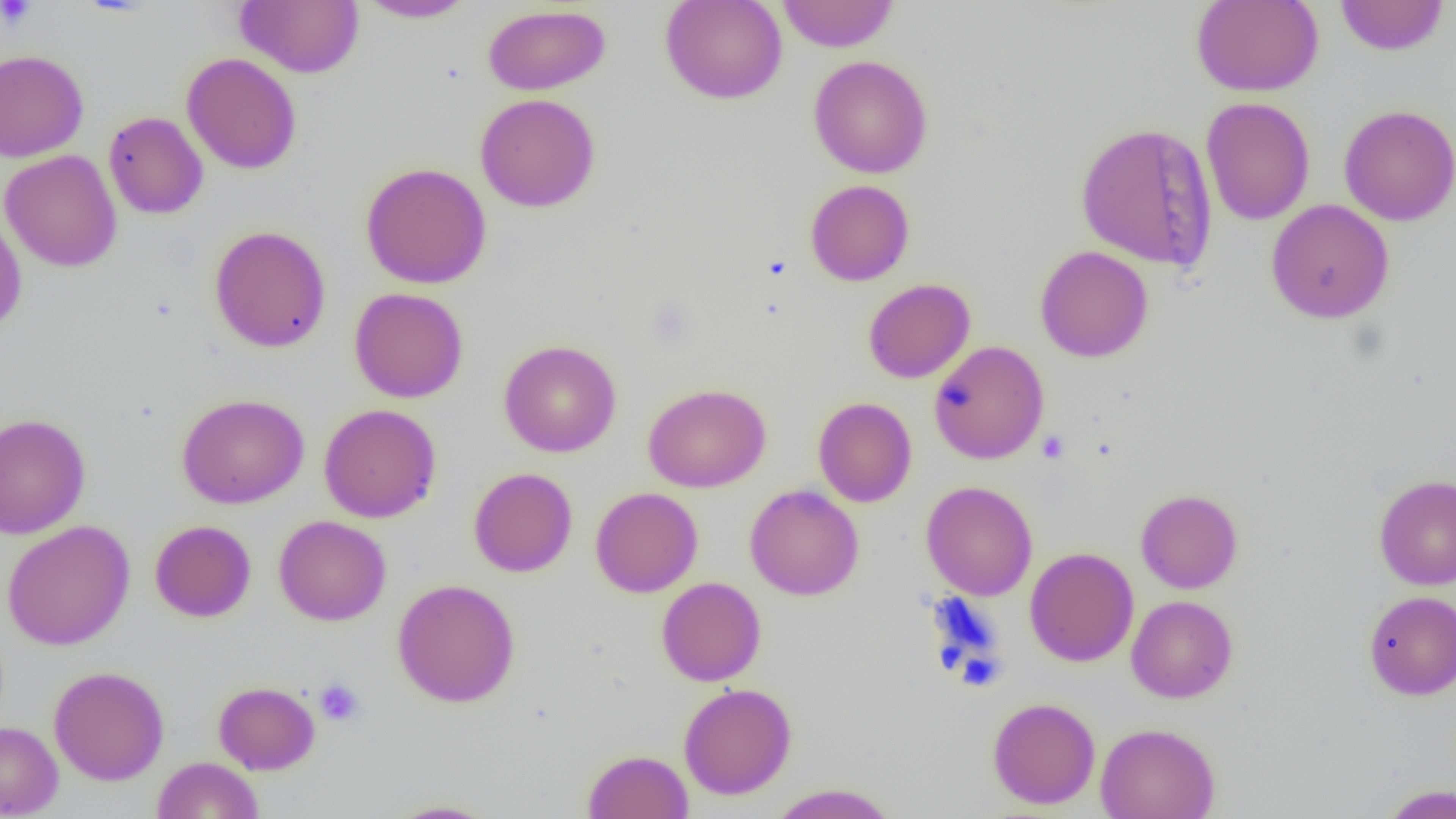

Summary:
  - Coordinate format: approximate bounding boxes as (x1,y1)-(x2,y2) corner pairs in pixels
  - Uninfected red blood cell locations: (236,0)-(363,78), (660,0)-(787,104), (777,0)-(899,52), (1191,0)-(1324,97), (1335,0)-(1449,56), (358,1)-(476,23), (482,4)-(610,95), (0,50)-(89,162), (182,53)-(302,174), (808,56)-(933,178), (475,93)-(601,212), (1200,97)-(1315,226), (1338,105)-(1456,226), (104,111)-(208,219), (1074,121)-(1219,271), (1,150)-(122,272), (360,162)-(492,289), (805,180)-(915,286), (1266,199)-(1395,324), (0,210)-(27,334), (209,225)-(331,352), (1035,245)-(1153,362), (863,278)-(975,383), (349,287)-(469,403), (499,340)-(621,458), (929,340)-(1049,464), (643,383)-(771,493), (176,393)-(309,509), (813,397)-(917,507), (319,403)-(441,522), (0,413)-(90,539), (469,468)-(577,577), (1373,473)-(1456,590), (921,481)-(1037,600), (744,484)-(864,600), (590,487)-(703,597), (1135,489)-(1243,593), (274,515)-(391,625), (150,519)-(256,622), (2,520)-(135,650), (1024,547)-(1139,667), (656,577)-(766,686), (392,578)-(521,707), (1363,591)-(1456,700), (1126,595)-(1238,703), (48,666)-(169,785), (213,681)-(321,775), (678,682)-(797,800), (987,697)-(1100,809), (0,721)-(63,817), (1094,722)-(1220,819), (582,749)-(694,819), (152,756)-(264,819), (767,783)-(900,819), (1380,784)-(1456,818), (383,799)-(500,818)
  - Platelet locations: (1,0)-(37,30), (1036,430)-(1070,463), (314,678)-(364,726)
  - Slide-level diagnosis: no evidence of blood parasites
  - Field of view: one of a larger specimen
  - Image size: 1456×819 pixels
  - Modality: light microscopy
  - Preparation: thin blood film
  - Magnification: 1000x